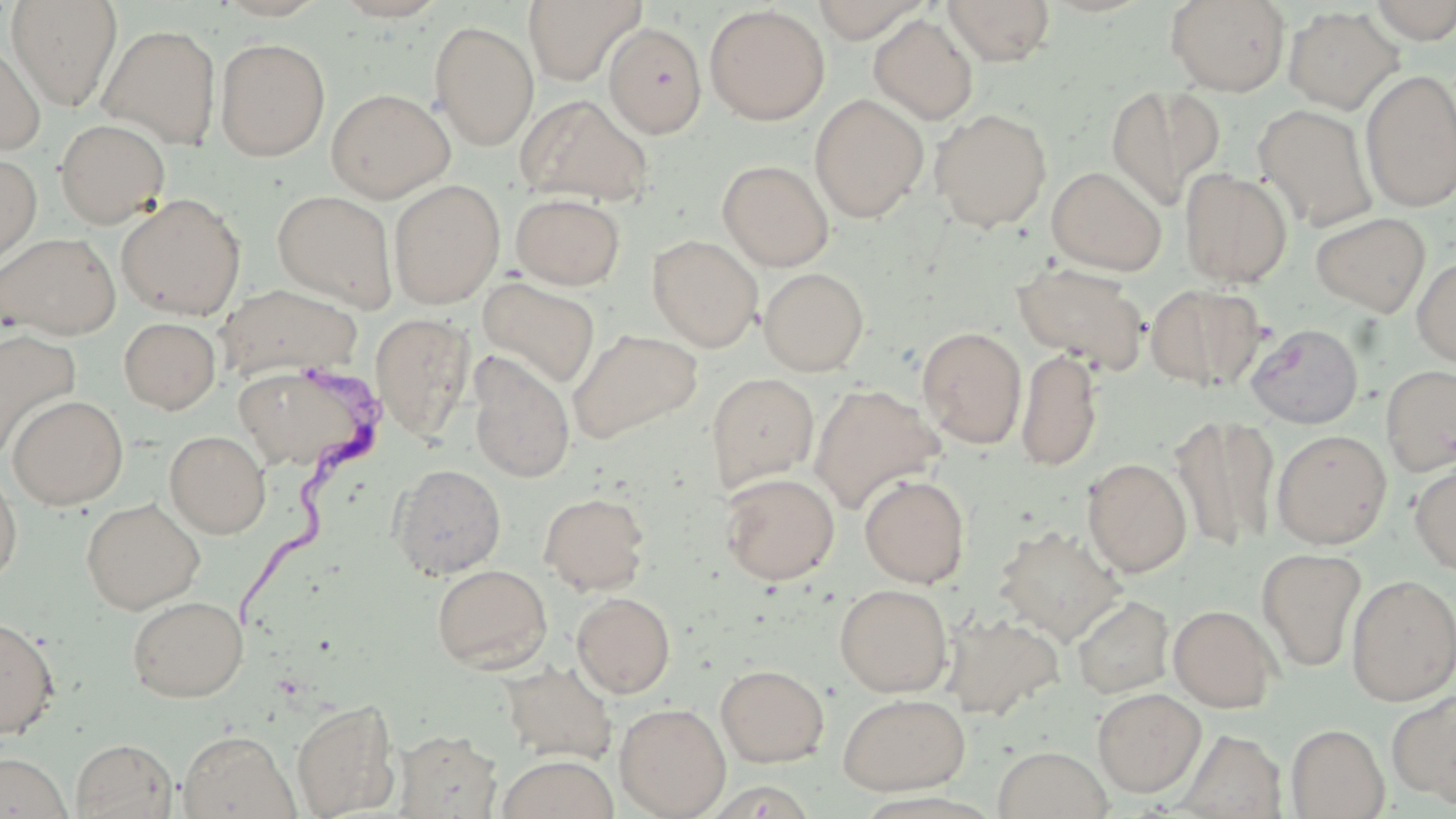

Summary:
  - Coordinate format: approximate bounding boxes as [x1, y1, x2, y2] in pixels
  - Uninfected red blood cell locations: [213, 0, 330, 21], [331, 0, 449, 21], [523, 0, 645, 86], [808, 0, 932, 43], [942, 0, 1056, 66], [1165, 0, 1290, 96], [1366, 0, 1456, 43], [6, 1, 122, 111], [704, 5, 830, 125], [1283, 6, 1402, 114], [869, 14, 978, 125], [429, 20, 539, 150], [605, 23, 707, 138], [98, 24, 221, 149], [0, 38, 45, 155], [216, 38, 330, 161], [1360, 70, 1456, 211], [1104, 84, 1223, 211], [326, 88, 454, 202], [516, 93, 654, 207], [809, 94, 928, 222], [1254, 103, 1378, 232], [930, 108, 1052, 232], [54, 118, 171, 228], [0, 153, 42, 268], [717, 160, 834, 271], [1046, 166, 1167, 275], [1179, 168, 1292, 287], [388, 179, 505, 308], [272, 189, 398, 311], [510, 192, 626, 290], [116, 193, 246, 320], [1310, 212, 1431, 316], [1, 232, 121, 340], [647, 235, 762, 352], [1412, 256, 1456, 367], [1012, 262, 1150, 374], [758, 267, 869, 376], [477, 276, 601, 390], [215, 283, 364, 382], [1146, 283, 1266, 391], [370, 312, 475, 442], [119, 317, 221, 414], [1245, 323, 1364, 429], [917, 326, 1027, 448], [568, 328, 702, 444], [0, 330, 81, 459], [1016, 347, 1102, 472], [468, 353, 575, 484], [235, 362, 383, 476], [1380, 364, 1456, 476], [705, 373, 820, 494], [808, 383, 944, 514], [7, 395, 128, 509], [1171, 414, 1280, 552], [1271, 429, 1392, 549], [164, 430, 271, 538], [1410, 457, 1456, 577], [1082, 458, 1192, 578], [0, 462, 22, 587], [390, 463, 507, 579], [719, 472, 840, 585], [859, 474, 970, 588], [538, 491, 651, 595], [81, 498, 205, 614], [994, 525, 1126, 645], [1257, 547, 1366, 673], [431, 564, 551, 673], [1346, 574, 1456, 706], [834, 583, 953, 697], [571, 592, 676, 698], [127, 595, 249, 702], [1071, 595, 1174, 699], [1167, 604, 1281, 712], [942, 611, 1065, 721], [0, 617, 60, 738], [500, 660, 616, 765], [715, 663, 829, 767], [1092, 688, 1206, 797], [1387, 691, 1456, 805], [838, 693, 971, 795], [291, 699, 400, 818], [614, 702, 731, 818], [1286, 724, 1389, 818], [178, 730, 298, 819], [1178, 730, 1289, 819], [394, 731, 502, 817], [71, 738, 177, 819], [992, 746, 1113, 819], [0, 751, 73, 819], [497, 754, 618, 819]
  - Trypanosoma brucei locations: [227, 357, 389, 627]
  - Slide-level diagnosis: Trypanosoma brucei
  - Modality: light microscopy
  - Image size: 1456×819 pixels
  - Field of view: single
  - Preparation: thin blood film
  - Magnification: 1000x
  - Stain: May-Grünwald-Giemsa